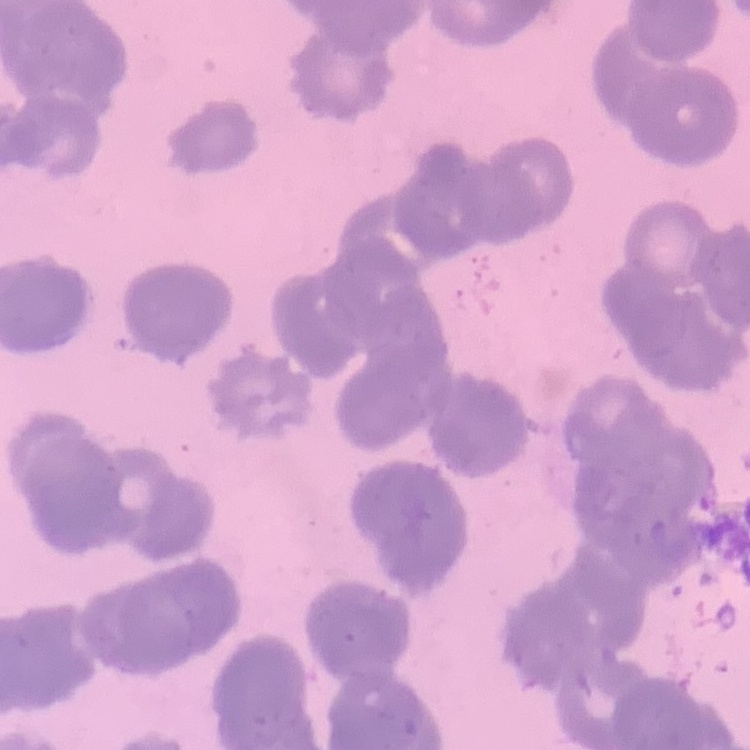 The red blood cells show rouleaux formation. One tile cut from a larger photomicrograph. Stained with either Field's or Giemsa. Thin blood smear.